Assess this cell for malaria.
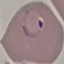
It is parasitized.

Thin blood film. Photographed with a smartphone camera at the microscope eyepiece. Giemsa stain. Automatically extracted cell patch, resized to 64 × 64 pixels.